Name the parasite shown.
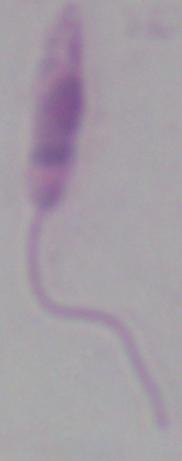
This is Leishmania.

{
  "magnification": "1000x",
  "modality": "micrograph"
}